Identify the parasite.
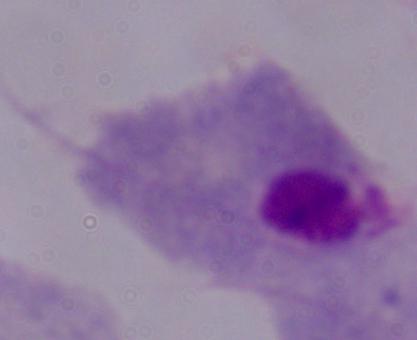

A trichomonad.

1000x magnification. Photomicrograph.